Comment on the morphology of the erythrocytes.
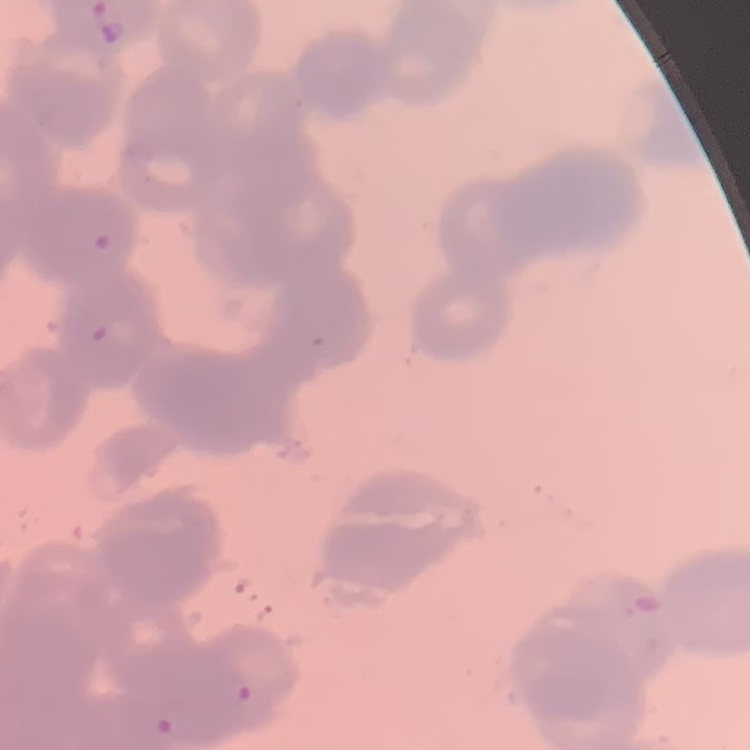

They show rouleaux formation.

Thin peripheral smear. Field's or Giemsa stain. One tile cut from a larger photomicrograph.